Assess this cell for malaria.
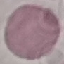
Uninfected.

stain = Giemsa
capture = smartphone through the microscope eyepiece
preparation = thin smear
image type = cell patch, automatically extracted from a larger field of view and resized to 64 × 64 pixels